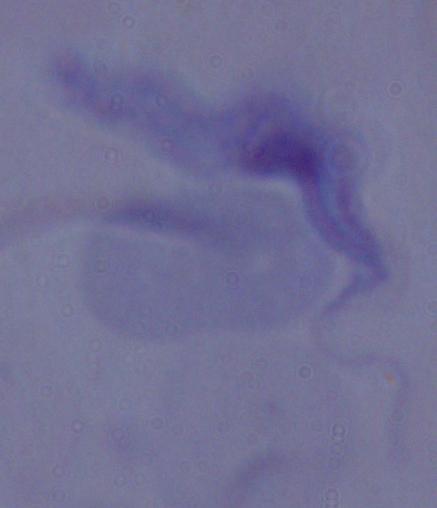

A trypanosome is shown. Micrograph. 1000x magnification.